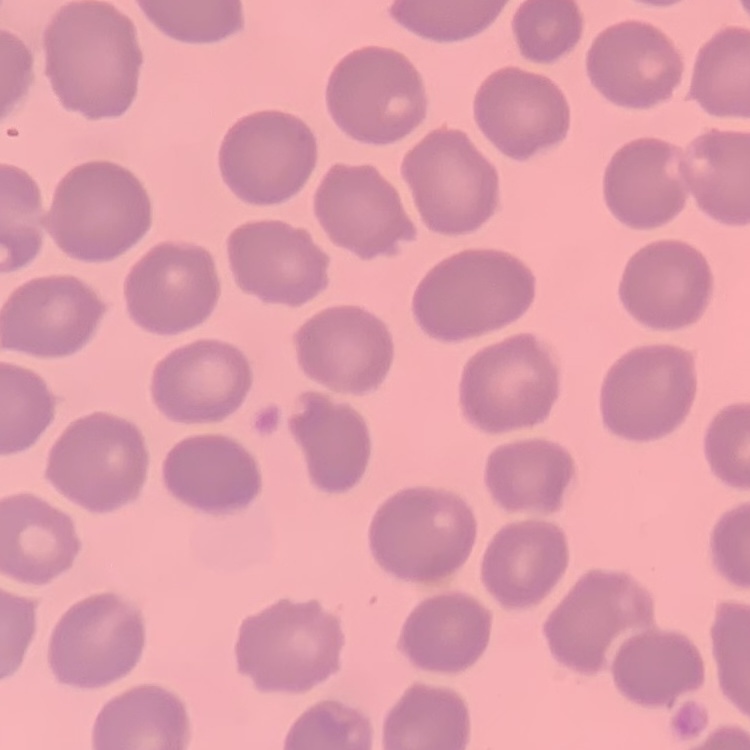

The erythrocytes exhibit no rouleaux formation. One tile cut from a larger photomicrograph. Thin peripheral smear. Stained with either Field's or Giemsa.